Classify this cell by malaria status.
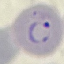
It is parasitized.

Acquired by smartphone through the microscope eyepiece. Automatically extracted cell patch, resized to 64 × 64 pixels. Giemsa stain. Thin smear of blood.